Identify the parasite.
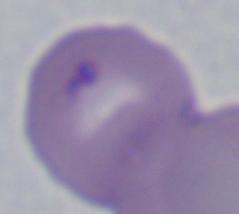
Babesia.

magnification = 1000x
modality = micrograph